Classify this cell by malaria status.
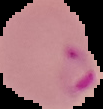

It is parasitized.

Summary:
  - Image type: segmented cell region with the area outside set to black
  - Preparation: thin blood smear
  - Image size: 103×109 pixels